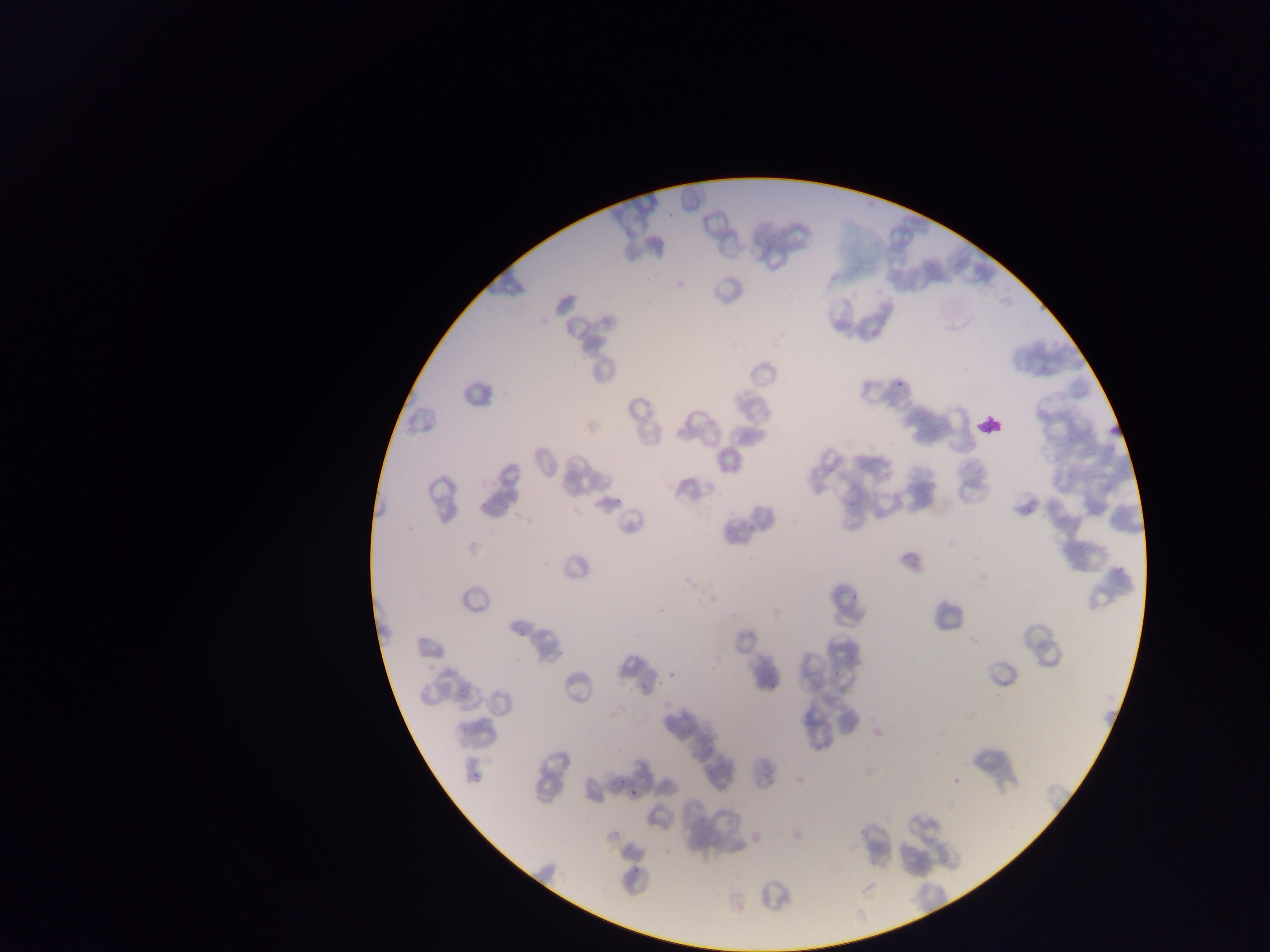

leukocyte locations = approximate bounding boxes as left top right bottom in pixels: 975 410 1005 439
country = Ghana
capture = mobile-phone photograph through a microscope
field of view = single
preparation = thin blood film
image size = 1270×952 pixels
malaria parasite locations = approximate bounding boxes as left top right bottom in pixels: 894 374 911 389; 613 496 626 503; 850 593 863 603; 515 626 528 636; 640 675 653 693; 616 775 628 784; 629 790 642 801